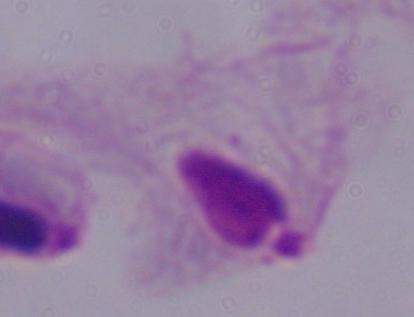

Photomicrograph. A trichomonad is shown. 1000x magnification.